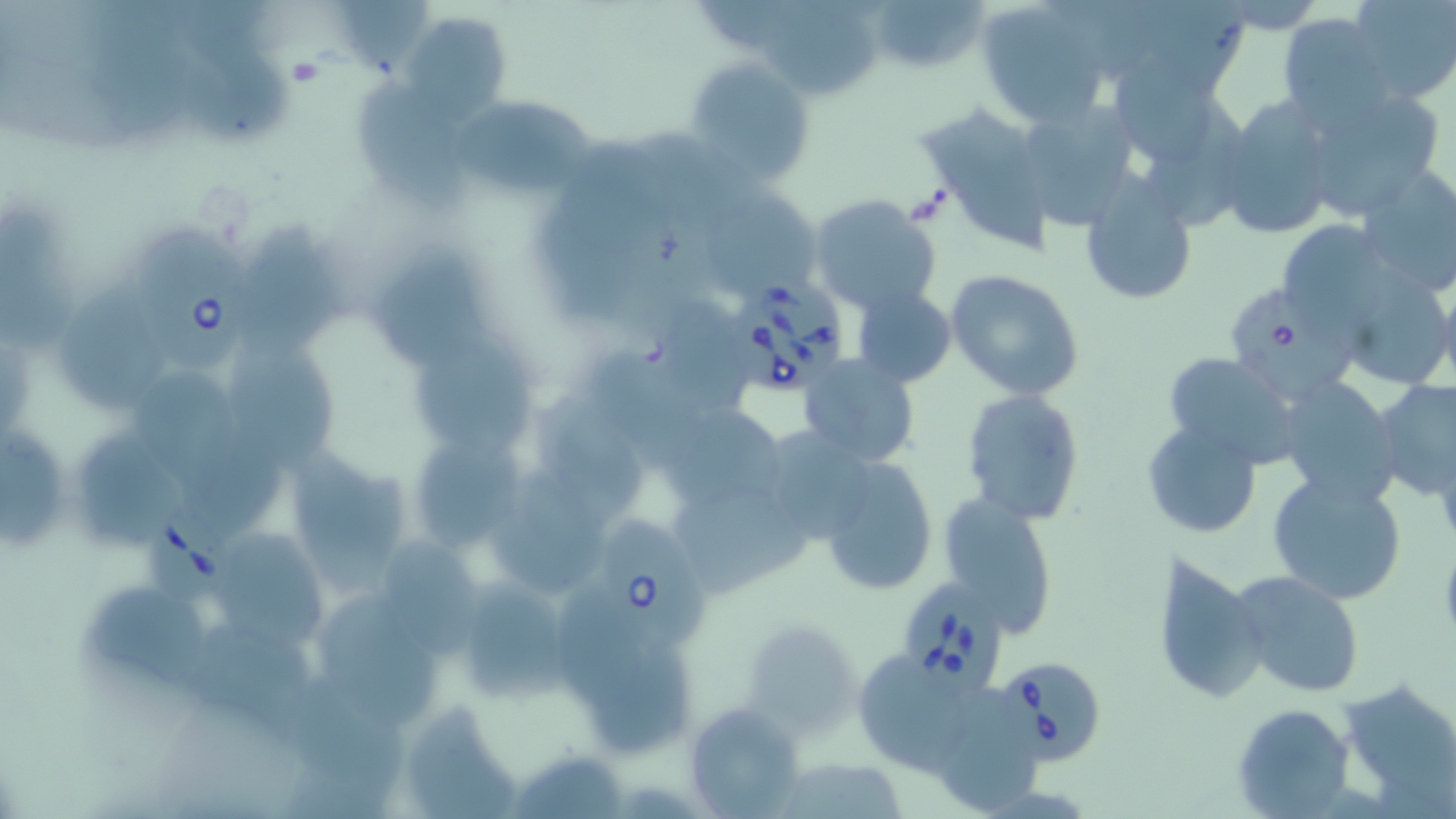
slide-level diagnosis = Babesia divergens
modality = optical microscopy
uninfected red blood cell locations = approximate bounding boxes as (x1,y1)-(x2,y2) corner pairs in pixels: (876,0)-(989,68), (1108,0)-(1255,100), (1347,0)-(1456,104), (976,1)-(1110,128), (758,5)-(884,101), (403,11)-(512,124), (1279,15)-(1396,126), (684,56)-(815,189), (1107,58)-(1228,168), (354,73)-(474,212), (1300,87)-(1447,219), (1215,93)-(1339,240), (913,98)-(1057,253), (449,99)-(599,197), (1019,100)-(1140,229), (638,129)-(768,237), (544,135)-(649,332), (1354,163)-(1456,295), (1080,176)-(1198,304), (701,187)-(817,298), (808,194)-(943,317), (0,203)-(81,352), (1283,223)-(1385,327), (240,228)-(353,362), (368,235)-(491,368), (1354,258)-(1450,380), (944,269)-(1086,400), (1433,274)-(1456,392), (68,281)-(176,414), (851,286)-(958,388), (665,296)-(759,420), (407,344)-(532,461), (597,350)-(709,472), (1161,351)-(1303,468), (799,353)-(920,467), (237,354)-(342,472), (136,367)-(247,497), (1276,378)-(1402,507), (1374,379)-(1456,499), (960,387)-(1086,525), (533,390)-(641,513), (658,402)-(787,514), (1143,419)-(1264,540), (0,429)-(72,551), (407,430)-(524,554), (765,431)-(874,544), (87,435)-(189,547), (286,450)-(416,588), (820,456)-(938,596), (495,459)-(605,597), (1267,472)-(1408,606), (666,487)-(814,600), (937,494)-(1059,633), (207,526)-(336,647), (383,543)-(491,661), (1153,553)-(1263,705), (1230,568)-(1365,697), (466,570)-(575,703), (95,587)-(213,692), (559,588)-(647,719), (318,596)-(447,720), (742,619)-(859,734), (190,621)-(322,743), (594,647)-(705,755), (862,653)-(961,766), (292,673)-(407,790), (1336,678)-(1456,811), (944,684)-(1050,812), (405,703)-(523,819), (683,703)-(807,816), (1231,703)-(1355,816), (515,747)-(631,819)
stain = May-Grünwald-Giemsa
field of view = single
magnification = 1000x
preparation = thin blood smear
image size = 1456×819 pixels
platelet locations = approximate bounding boxes as (x1,y1)-(x2,y2) corner pairs in pixels: (288,56)-(320,86)
Babesia divergens-infected red blood cell locations = approximate bounding boxes as (x1,y1)-(x2,y2) corner pairs in pixels: (134,230)-(251,364), (726,273)-(851,398), (1231,289)-(1357,401), (143,502)-(228,599), (595,511)-(705,648), (897,582)-(1007,697), (995,655)-(1109,764)